Describe the morphology of the erythrocytes.
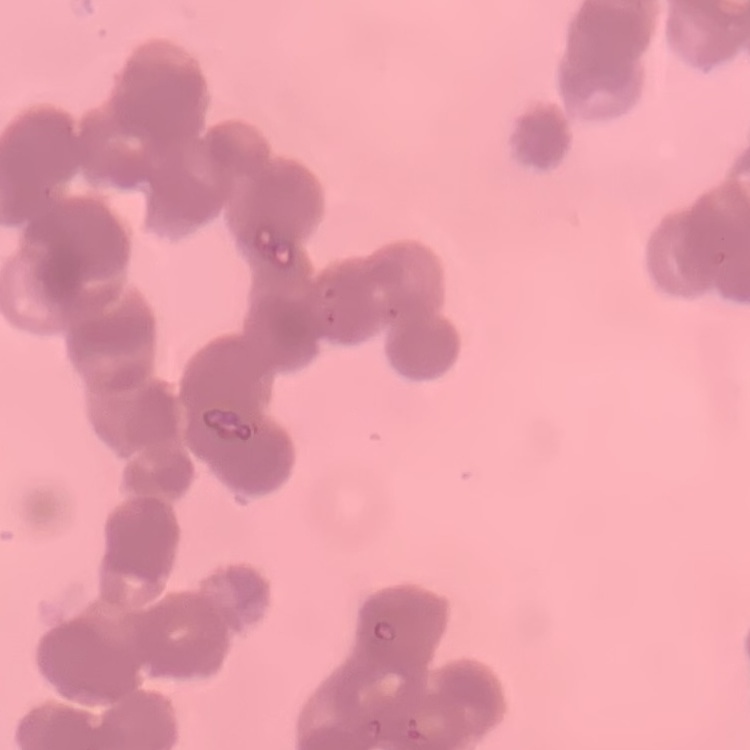
They show rouleaux formation.

Summary:
  - Image type: one tile cut from a larger photomicrograph
  - Preparation: thin peripheral smear
  - Stain: Field's or Giemsa